State which parasite is depicted.
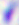
This is Toxoplasma gondii.

modality = photomicrograph
magnification = 400x